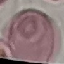
malaria status = uninfected
capture = smartphone through the microscope eyepiece
preparation = thin blood film
stain = Giemsa
image type = automatically extracted cell patch, resized to 64 × 64 pixels